Report the malaria status of this cell.
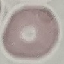
It is uninfected.

Thin blood film. Cell patch, automatically extracted from a larger field of view and resized to 64 × 64 pixels. Giemsa stain. Photographed with a smartphone camera at the microscope eyepiece.